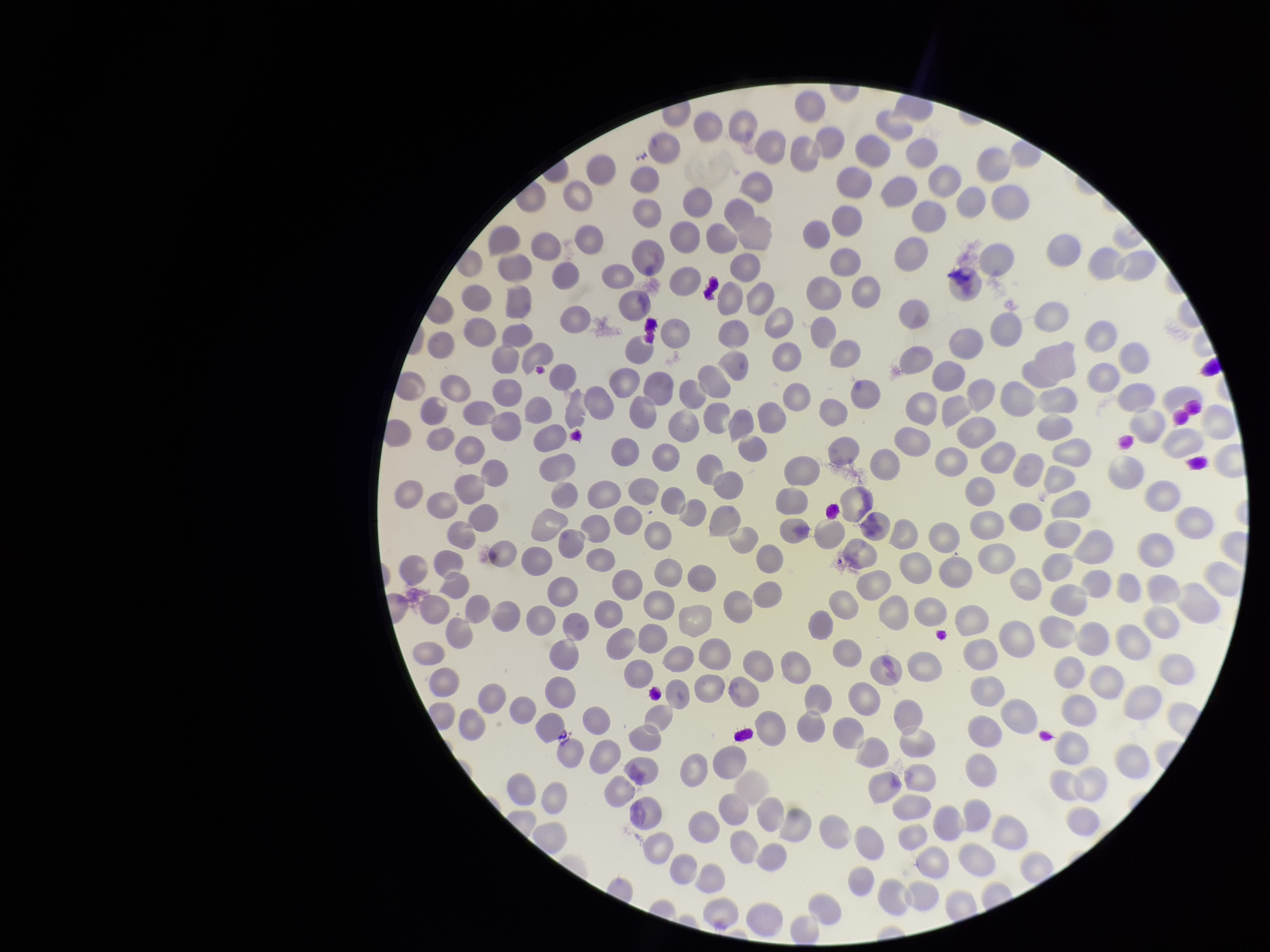

Parasitized red blood cells: none detected. Smartphone photograph taken through the eyepiece of a microscope. Single field of view. Image is 1270×952 pixels. Giemsa stain. Patient malaria status: negative. Parasitized red blood cell count: 0. Preparation: thin smear. Red blood cell count: 276.